State which parasite is depicted.
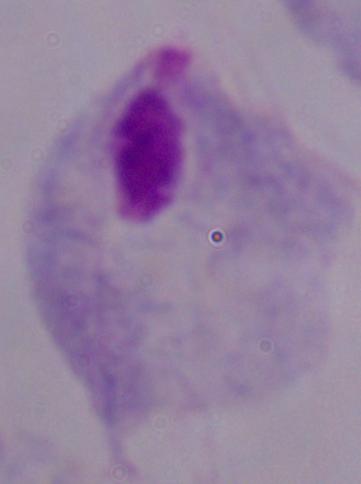

A trichomonad.

modality = photomicrograph
magnification = 1000x